Report the malaria status of this cell.
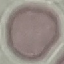
It is uninfected.

preparation = thin smear
image type = automatically extracted cell patch, resized to 64 × 64 pixels
stain = Giemsa
capture = smartphone through the microscope eyepiece